Evaluate for Plasmodium parasites.
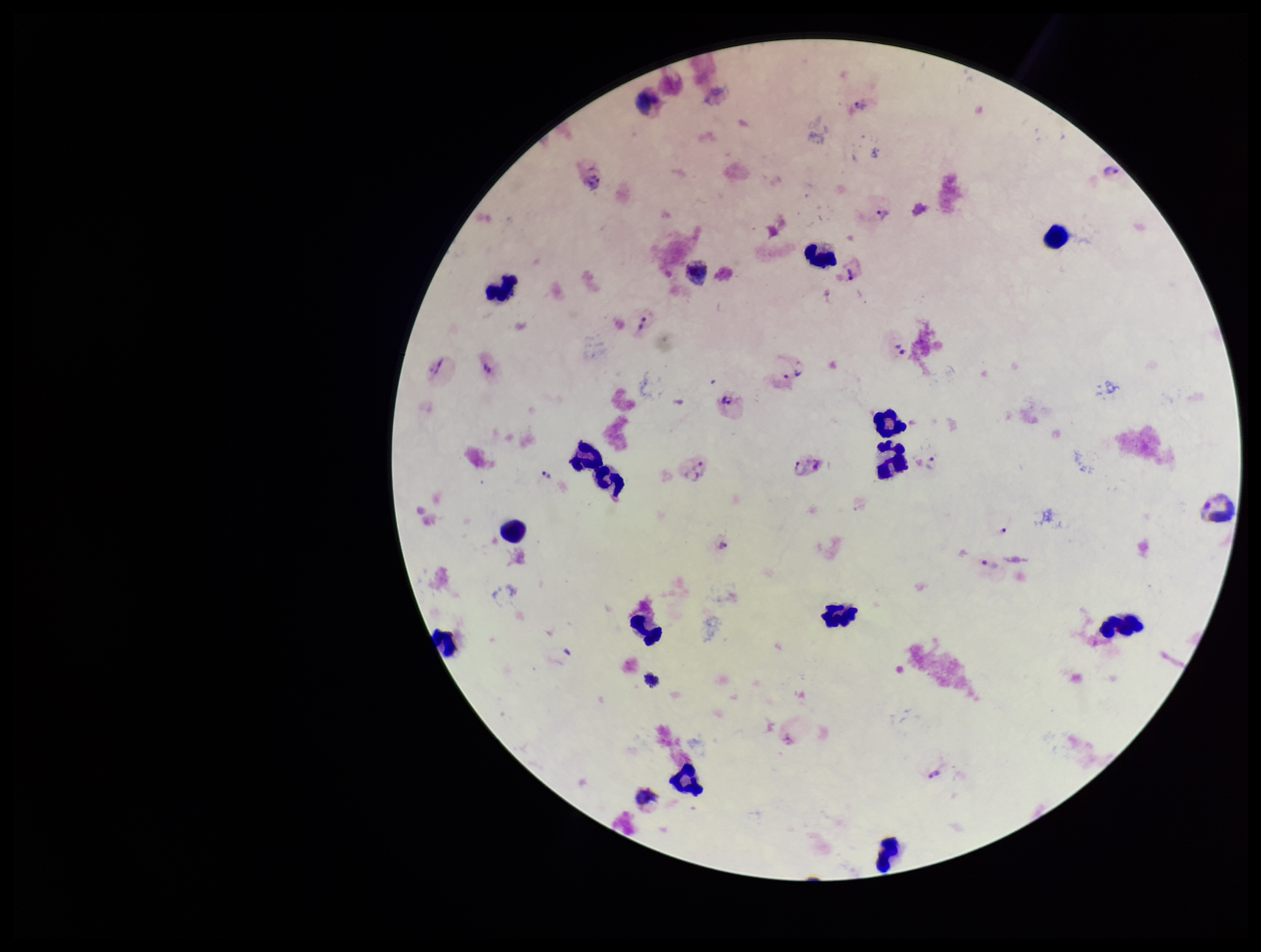
Identified.

Summary:
  - Species reported for this patient: Plasmodium vivax
  - Parasite count: 23
  - Patient malaria status: positive
  - Stain: Giemsa
  - Capture: smartphone photograph through the microscope eyepiece
  - Image size: 1261×952 pixels
  - Preparation: thick
  - Field of view: one from this slide
  - Leukocyte count: 18